State which parasite is depicted.
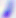

Toxoplasma gondii.

Summary:
  - Magnification: 400x
  - Modality: micrograph